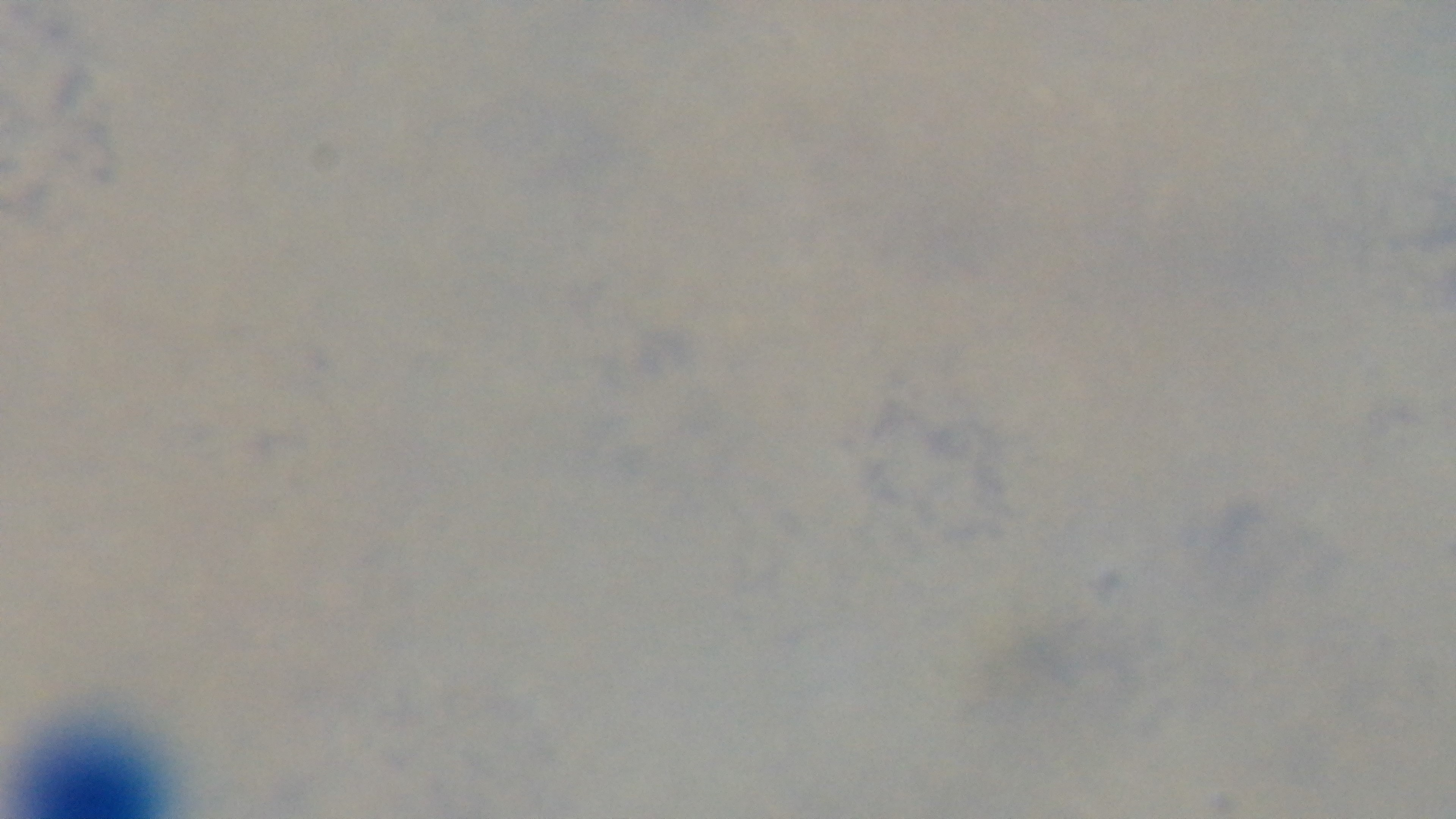

Single field of view. Malaria status: uninfected. Giemsa stain. Preparation: thick blood film. Captured with a mounted 4K digital camera. Oil-immersion objective, 100x. Photomicrograph.